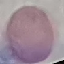

Summary:
  - Malaria status: uninfected
  - Preparation: thin smear
  - Stain: Giemsa
  - Capture: smartphone camera at the microscope eyepiece
  - Image type: cell patch, automatically extracted from a larger field of view and resized to 64 × 64 pixels